Classify this cell by malaria status.
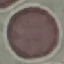

Uninfected.

preparation: thin blood smear
stain: Giemsa
image_type: automatically extracted cell patch, resized to 64 × 64 pixels
capture: smartphone camera at the microscope eyepiece